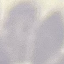

result = no malaria parasites seen
preparation = thin blood film
image type = cell patch, automatically extracted from a larger field of view and resized to 64 × 64 pixels
stain = Giemsa
capture = smartphone through the microscope eyepiece